Locate and identify every blood parasite.
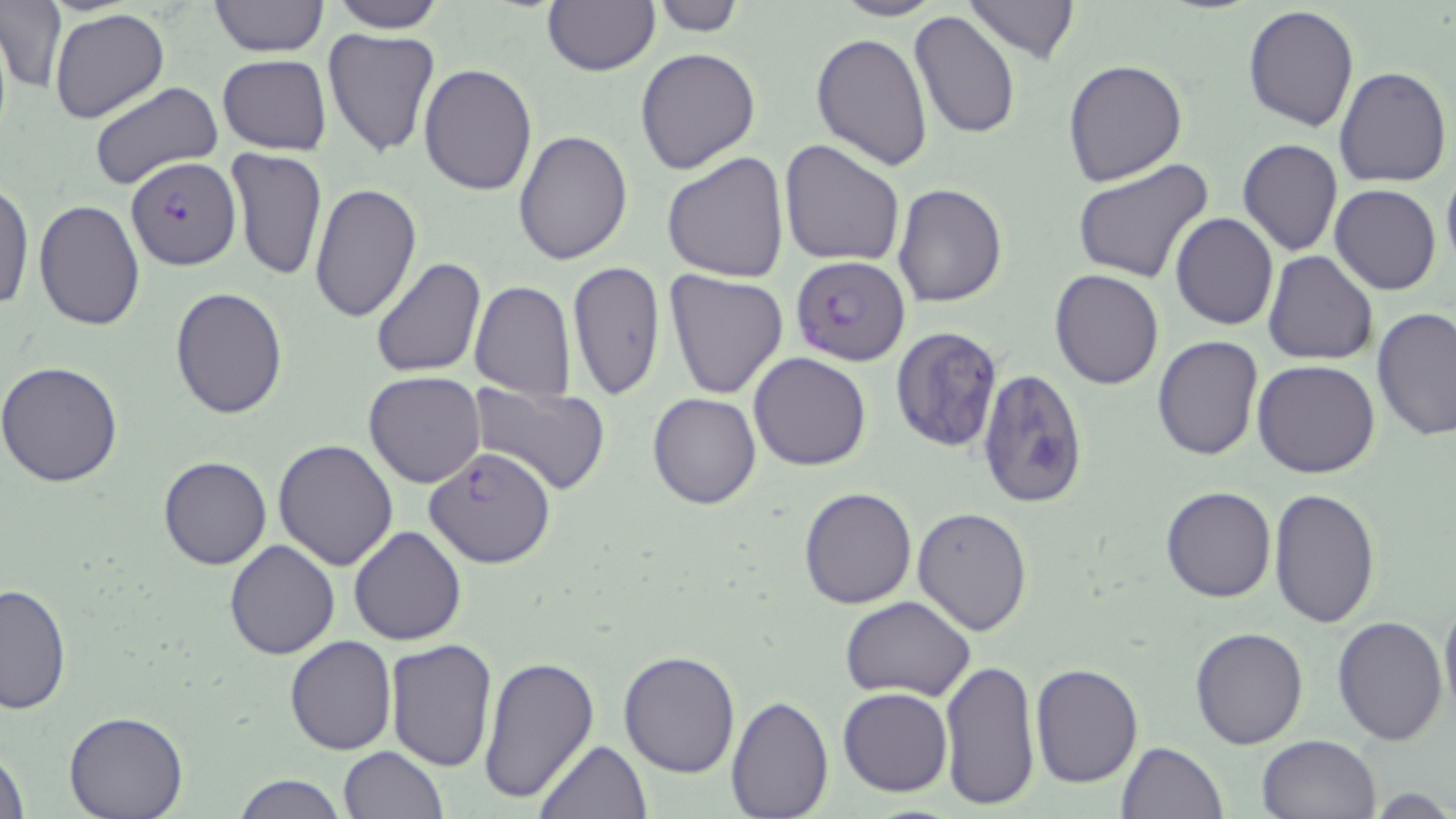
Approximate bounding boxes as [x1, y1, x2, y2] in pixels.
Plasmodium falciparum-infected red blood cells: [125, 157, 240, 270], [789, 256, 910, 365], [424, 446, 556, 568].
No Plasmodium ovale, Plasmodium malariae, Plasmodium vivax, Babesia divergens, or Trypanosoma brucei observed.

Summary:
  - Uninfected red blood cell locations: [208, 0, 328, 57], [326, 0, 449, 33], [541, 0, 659, 75], [650, 0, 747, 36], [833, 0, 943, 21], [961, 0, 1081, 64], [1, 4, 66, 94], [1242, 6, 1361, 131], [50, 10, 167, 124], [909, 10, 1023, 141], [322, 27, 442, 159], [811, 32, 932, 171], [635, 47, 761, 176], [217, 55, 331, 155], [1062, 58, 1189, 188], [419, 63, 537, 195], [1333, 67, 1451, 189], [90, 82, 223, 188], [511, 131, 633, 265], [778, 139, 906, 266], [1236, 139, 1343, 255], [224, 148, 328, 285], [661, 151, 789, 283], [1072, 158, 1214, 283], [225, 164, 424, 301], [1441, 165, 1456, 273], [0, 178, 33, 314], [311, 182, 421, 325], [892, 183, 1008, 308], [1331, 185, 1442, 295], [33, 200, 145, 330], [1170, 212, 1278, 329], [1261, 250, 1378, 366], [371, 256, 487, 376], [566, 261, 665, 400], [662, 268, 789, 399], [1050, 270, 1163, 390], [468, 281, 576, 400], [170, 286, 288, 419], [1371, 307, 1454, 443], [891, 324, 1003, 453], [1152, 336, 1263, 462], [749, 352, 872, 472], [0, 360, 125, 486], [1253, 360, 1382, 478], [976, 369, 1090, 509], [363, 371, 486, 488], [466, 381, 612, 497], [647, 392, 762, 511], [273, 441, 399, 570], [157, 457, 270, 570], [798, 486, 918, 609], [1161, 486, 1277, 604], [1266, 489, 1382, 630], [913, 506, 1033, 635], [349, 525, 466, 645], [224, 539, 339, 659], [0, 583, 72, 715], [1439, 589, 1456, 722], [841, 596, 975, 700], [1333, 614, 1448, 745], [1189, 627, 1309, 748], [283, 635, 397, 755], [384, 640, 498, 772], [617, 650, 742, 777], [479, 656, 599, 805], [939, 657, 1041, 810], [1030, 663, 1142, 788], [838, 688, 953, 796], [725, 695, 831, 815], [66, 711, 186, 819], [1258, 734, 1382, 819], [535, 739, 651, 818], [1116, 741, 1228, 819], [0, 745, 31, 819], [337, 746, 447, 818], [232, 775, 345, 818]
  - Slide-level diagnosis: Plasmodium falciparum
  - Magnification: 1000x
  - Preparation: thin blood film
  - Field of view: single
  - Stain: May-Grünwald-Giemsa
  - Image size: 1456×819 pixels
  - Modality: light microscopy